Assess this cell for malaria.
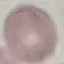
It is uninfected.

capture = smartphone through the microscope eyepiece
image type = automatically extracted cell patch, resized to 64 × 64 pixels
preparation = thin blood smear
stain = Giemsa